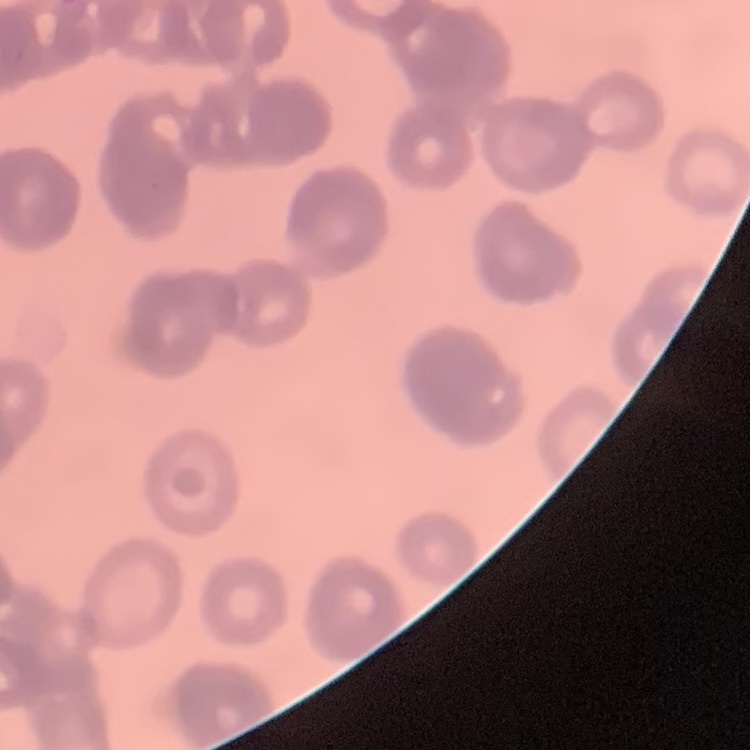
Summary:
  - Red blood cell morphology: rouleaux formation
  - Preparation: thin peripheral smear
  - Image type: square crop of a larger photomicrograph
  - Stain: Field's or Giemsa